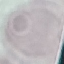
{
  "malaria_status": "uninfected",
  "image_type": "automatically extracted cell patch, resized to 64 × 64 pixels",
  "stain": "Giemsa",
  "preparation": "thin blood film",
  "capture": "smartphone through the microscope eyepiece"
}